Classify this cell by malaria status.
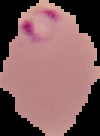

Parasitized.

image type = cell region segmented out of the field of view; surrounding area masked to black
image size = 100×136 pixels
preparation = thin blood film